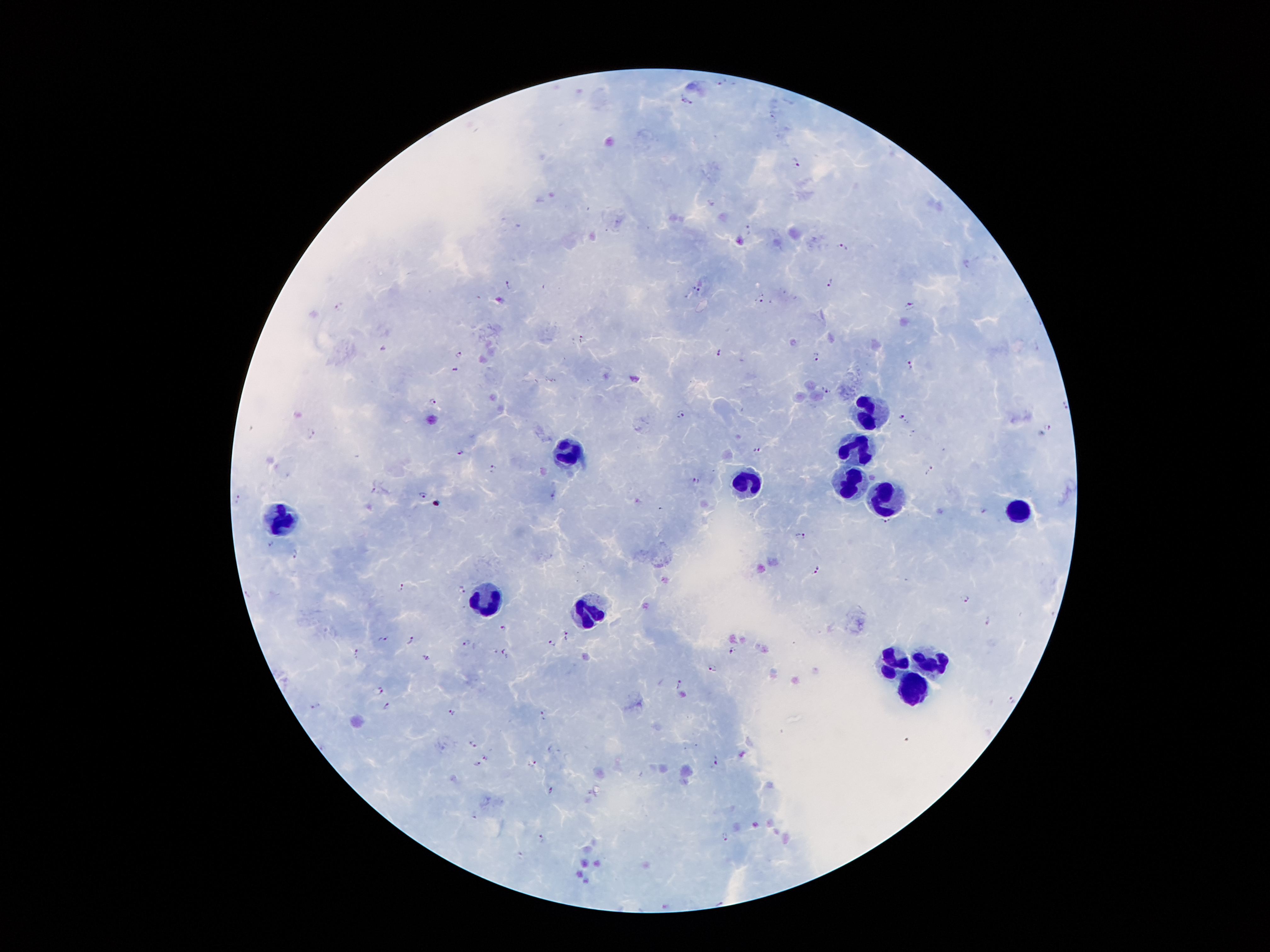
Approximate centers as [x, y] in pixels. Plasmodium parasite locations: [721, 79], [682, 100], [691, 102], [797, 163], [747, 229], [842, 247], [829, 282], [508, 284], [696, 288], [761, 299], [910, 306], [339, 307], [581, 338], [383, 347], [718, 352], [459, 355], [817, 356], [911, 365], [456, 370], [826, 388], [434, 401], [1064, 404], [680, 414], [901, 417], [1047, 429], [313, 433], [757, 450], [460, 452], [493, 468], [928, 470], [695, 480], [425, 495], [552, 496], [240, 499], [438, 504], [984, 511], [887, 522], [801, 535], [270, 546], [294, 553], [816, 571], [402, 587], [460, 590], [966, 599], [988, 624], [504, 627], [564, 633], [385, 640], [412, 641], [468, 643], [553, 644], [357, 650], [503, 651], [733, 651], [427, 658], [711, 669], [679, 685], [380, 690], [1010, 699], [387, 705], [315, 706], [452, 714], [542, 715], [474, 744], [486, 757], [717, 762], [534, 763], [478, 764], [551, 789], [726, 836], [541, 838]. Leukocyte locations: [867, 412], [864, 444], [571, 454], [753, 482], [850, 484], [882, 496], [1016, 510], [280, 518], [487, 602], [587, 611], [932, 659], [894, 661], [920, 687]. Thick blood smear. Giemsa-stained preparation. 100x magnification. Smartphone photograph taken through the microscope eyepiece. Single field of view. Image is 1270×952 pixels. Patient malaria status: infected with Plasmodium falciparum.